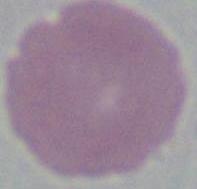
modality = micrograph
magnification = 1000x
identification = erythrocyte